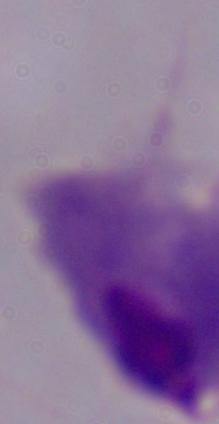 Micrograph. A trichomonad is seen. Captured at 1000x magnification.